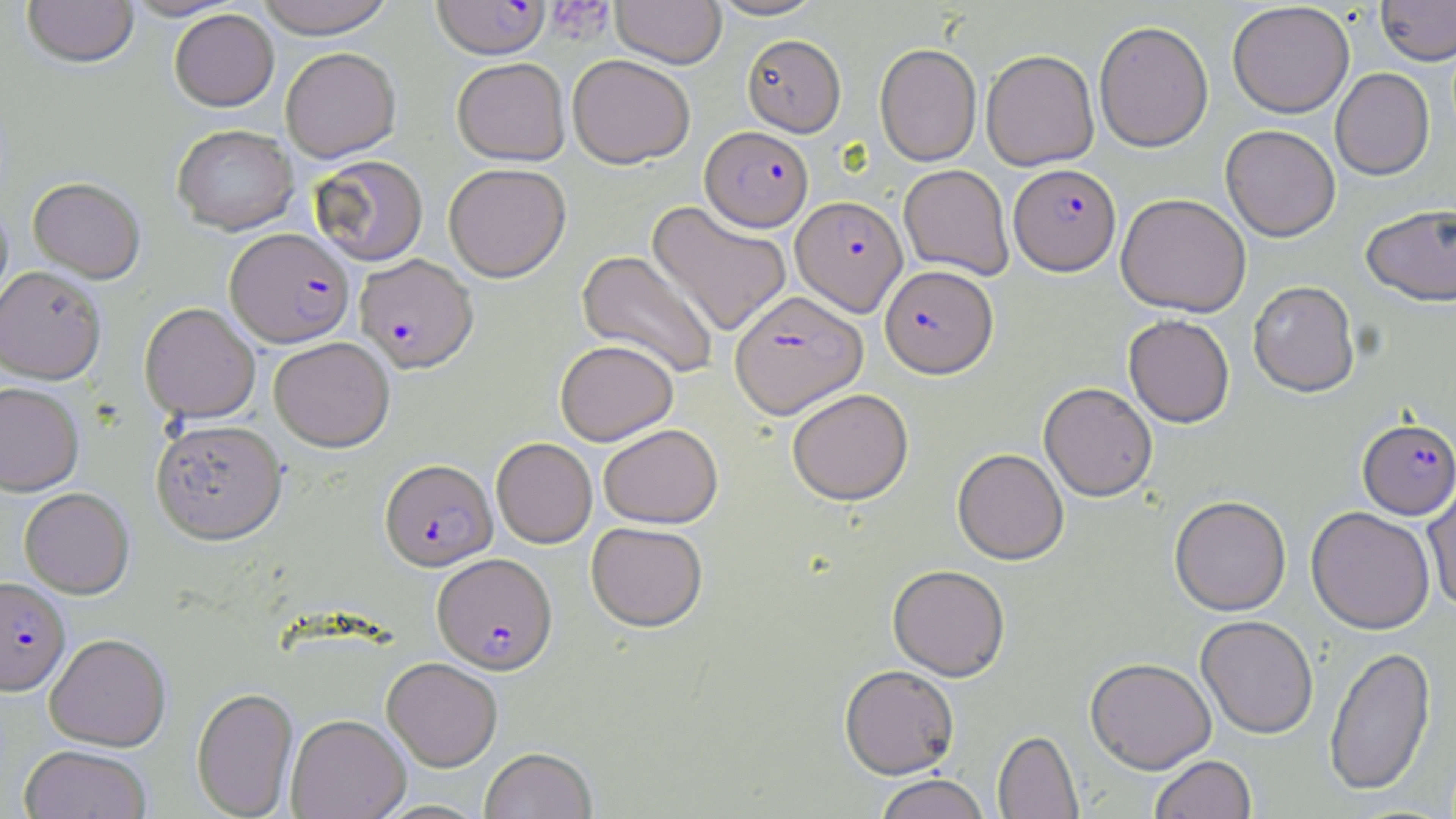

Summary:
  - Coordinate format: approximate bounding boxes as (x1, y1, x2, y2) in pixels
  - Plasmodium falciparum-infected red blood cell locations: (431, 1, 550, 59), (701, 126, 813, 231), (1009, 163, 1121, 275), (791, 195, 907, 315), (225, 227, 353, 348), (354, 254, 478, 373), (880, 264, 997, 378), (730, 290, 867, 418), (1358, 418, 1456, 519), (380, 459, 496, 570), (433, 552, 557, 674), (0, 577, 70, 695)
  - Platelet locations: (546, 1, 615, 44)
  - Uninfected red blood cell locations: (22, 0, 139, 68), (122, 0, 243, 21), (253, 0, 398, 38), (611, 0, 726, 68), (709, 0, 825, 20), (1376, 0, 1456, 65), (1227, 2, 1354, 118), (169, 9, 279, 111), (1094, 20, 1214, 152), (742, 34, 846, 136), (875, 42, 981, 166), (280, 47, 400, 163), (981, 49, 1099, 171), (567, 54, 695, 169), (452, 57, 570, 165), (1330, 67, 1435, 180), (172, 124, 299, 235), (1221, 125, 1340, 242), (309, 154, 428, 266), (443, 163, 571, 282), (899, 164, 1014, 280), (28, 177, 145, 283), (1116, 192, 1251, 317), (646, 200, 791, 337), (1361, 203, 1455, 306), (577, 250, 720, 380), (0, 266, 106, 383), (1247, 280, 1360, 397), (139, 302, 260, 423), (1123, 314, 1235, 428), (269, 337, 395, 451), (555, 339, 677, 445), (0, 382, 84, 496), (1039, 382, 1157, 501), (787, 388, 913, 505), (151, 418, 286, 543), (598, 423, 722, 528), (491, 437, 596, 547), (953, 448, 1068, 564), (1422, 476, 1456, 612), (19, 487, 134, 598), (1169, 495, 1291, 616), (1306, 506, 1435, 634), (587, 521, 708, 631), (888, 564, 1010, 681), (1195, 615, 1319, 739), (45, 633, 170, 751), (1324, 644, 1436, 797), (382, 657, 502, 770), (1085, 657, 1216, 774), (839, 664, 960, 779), (192, 687, 298, 817), (286, 714, 410, 819), (993, 730, 1083, 818), (19, 744, 152, 818), (480, 747, 597, 819), (1150, 754, 1256, 819), (873, 774, 990, 819)
  - Slide-level diagnosis: Plasmodium falciparum
  - Magnification: 1000x
  - Preparation: thin blood film
  - Stain: May-Grünwald-Giemsa
  - Field of view: one of a larger specimen
  - Modality: light microscopy
  - Image size: 1456×819 pixels